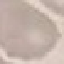
Summary:
  - Result: negative for malaria parasites
  - Image type: cell patch, automatically extracted from a larger field of view and resized to 64 × 64 pixels
  - Stain: Giemsa
  - Preparation: thin smear
  - Capture: smartphone camera at the microscope eyepiece